Classify this cell by malaria status.
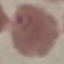

Parasitized.

preparation: thin blood film
capture: smartphone through the microscope eyepiece
image_type: automatically extracted cell patch, resized to 64 × 64 pixels
stain: Giemsa